State which parasite is depicted.
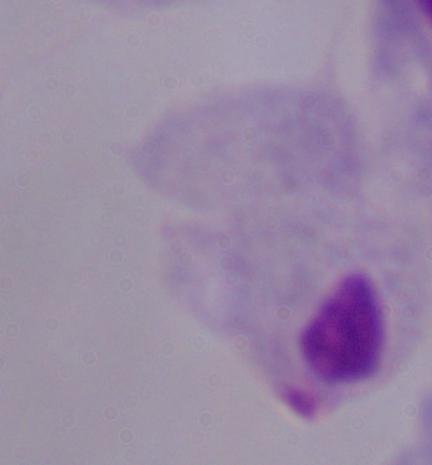
A trichomonad.

modality = photomicrograph
magnification = 1000x